Classify this cell by malaria status.
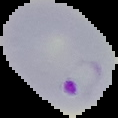
Parasitized.

Summary:
  - Preparation: thin blood smear
  - Image size: 118×118 pixels
  - Image type: cell region segmented out of the field of view; surrounding area masked to black